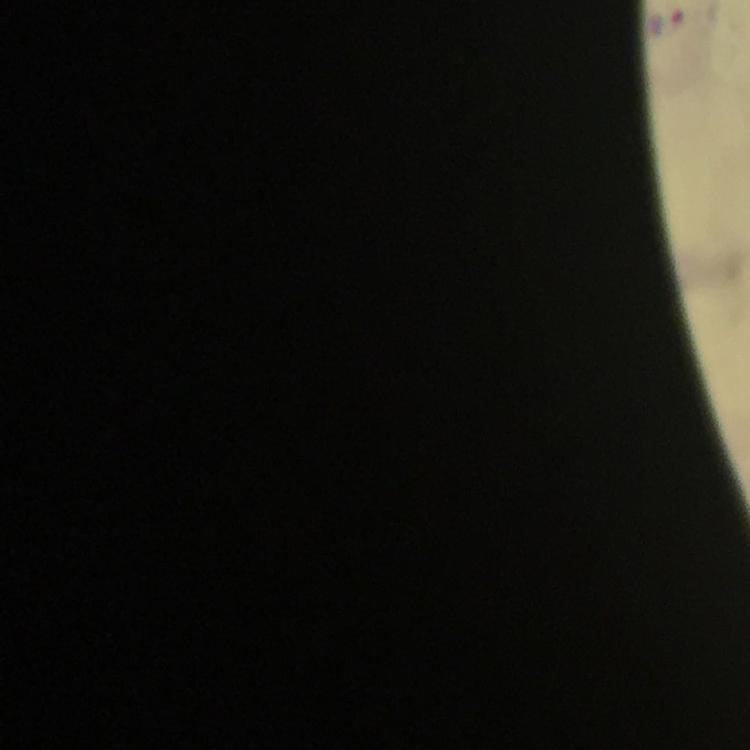
Approximate object centers, in pixels from the top-left corner.
Summary:
  - Malaria parasite locations: (x=667, y=21)
  - Stain: Giemsa
  - Immersion oil: applied
  - Magnification: 100x
  - Context: from a diagnostic examination for malaria
  - Capture: smartphone photograph through a microscope
  - Image size: 750×750 pixels
  - Preparation: thick blood film
  - Cropped from: a single field of view